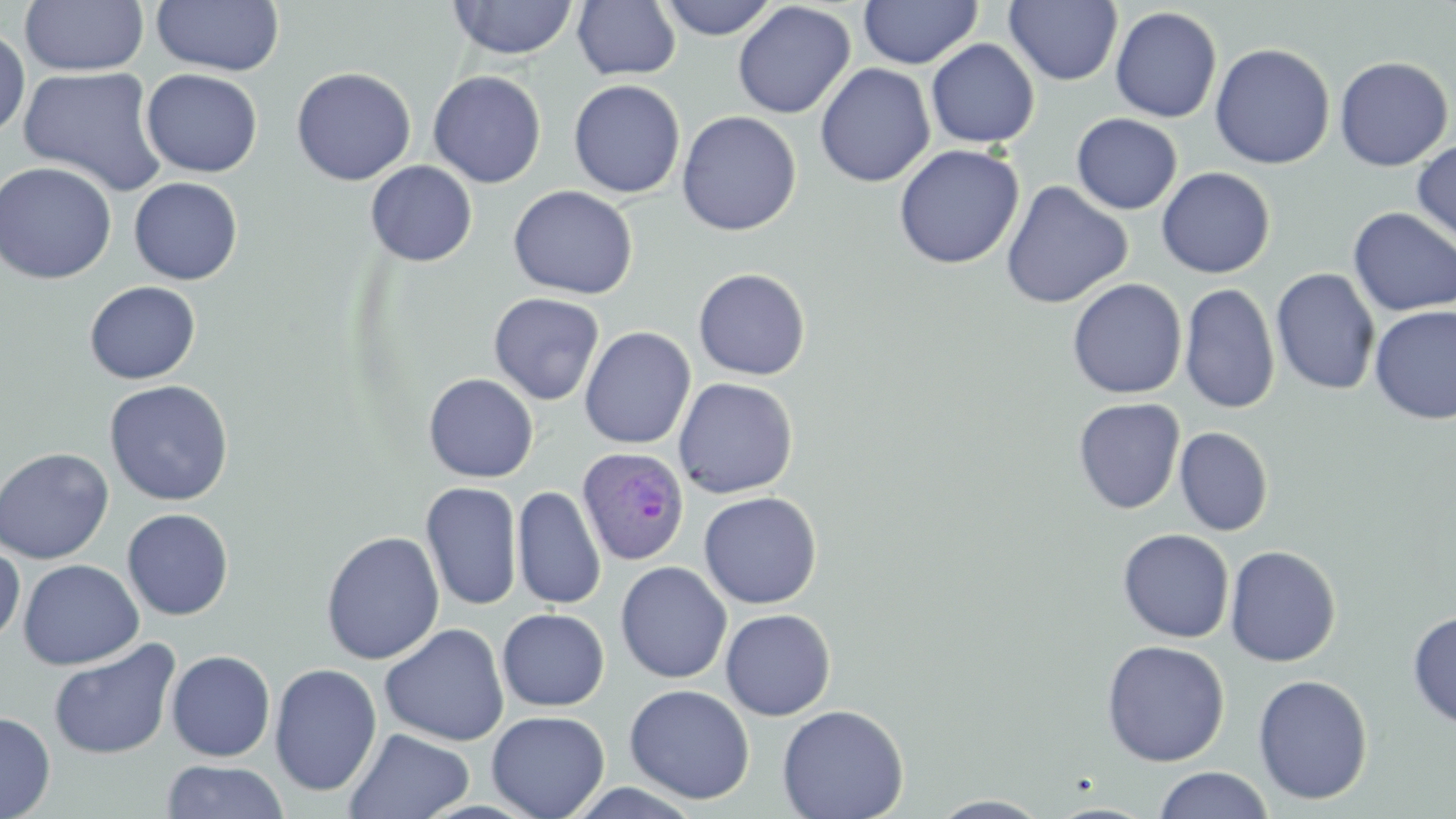 Approximate bounding boxes as [x1, y1, x2, y2] in pixels. Uninfected red blood cell locations: [20, 0, 148, 77], [448, 0, 579, 60], [658, 0, 779, 40], [858, 0, 983, 69], [151, 1, 285, 76], [572, 1, 681, 80], [1004, 1, 1123, 86], [732, 2, 856, 119], [1110, 6, 1222, 122], [0, 25, 30, 141], [925, 38, 1040, 148], [1210, 43, 1335, 169], [1333, 56, 1454, 171], [814, 63, 935, 188], [17, 65, 168, 196], [291, 66, 416, 186], [141, 68, 263, 177], [428, 70, 547, 189], [568, 79, 686, 199], [676, 110, 801, 236], [1071, 113, 1182, 214], [1412, 139, 1456, 248], [892, 143, 1025, 269], [365, 160, 478, 267], [0, 161, 117, 284], [1156, 167, 1275, 279], [129, 177, 243, 285], [1001, 180, 1133, 309], [508, 184, 638, 300], [499, 187, 616, 408], [1348, 207, 1456, 316], [692, 268, 811, 380], [1271, 268, 1381, 395], [1066, 278, 1187, 399], [84, 281, 201, 384], [1180, 283, 1280, 414], [488, 292, 605, 406], [1369, 305, 1456, 426], [579, 326, 696, 450], [423, 373, 539, 483], [673, 377, 799, 499], [104, 379, 234, 506], [1073, 397, 1185, 514], [1175, 427, 1273, 536], [0, 446, 114, 564], [420, 481, 522, 611], [512, 486, 606, 610], [698, 491, 822, 609], [122, 508, 234, 620], [1117, 529, 1235, 643], [320, 531, 445, 664], [0, 543, 25, 646], [1225, 545, 1341, 667], [18, 559, 144, 670], [615, 561, 732, 684], [496, 608, 610, 711], [720, 608, 836, 720], [1407, 611, 1456, 729], [380, 623, 509, 746], [48, 638, 180, 760], [1101, 639, 1230, 767], [166, 649, 276, 761], [269, 663, 382, 797], [1252, 674, 1374, 805], [623, 684, 755, 804], [777, 704, 909, 819], [486, 710, 610, 819], [0, 711, 56, 818], [344, 727, 474, 818], [160, 760, 291, 818], [1153, 766, 1275, 819], [929, 795, 1053, 818]. Plasmodium ovale-infected red blood cell locations: [576, 446, 691, 566]. Slide-level diagnosis: Plasmodium ovale. May-Grünwald-Giemsa-stained preparation. Light microscopy. Thin blood smear. One field of a larger specimen. Captured at 1000x magnification. Image is 1456×819 pixels.